Report the malaria status of this cell.
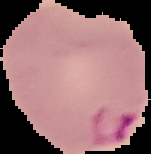

It is parasitized.

{
  "image_type": "segmented cell region on a black background",
  "image_size": "151×154 pixels",
  "preparation": "thin blood smear"
}